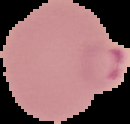
The area outside the segmented cell region is set to black. Image is 130×124 pixels. From a thin blood smear. Malaria status: parasitized.